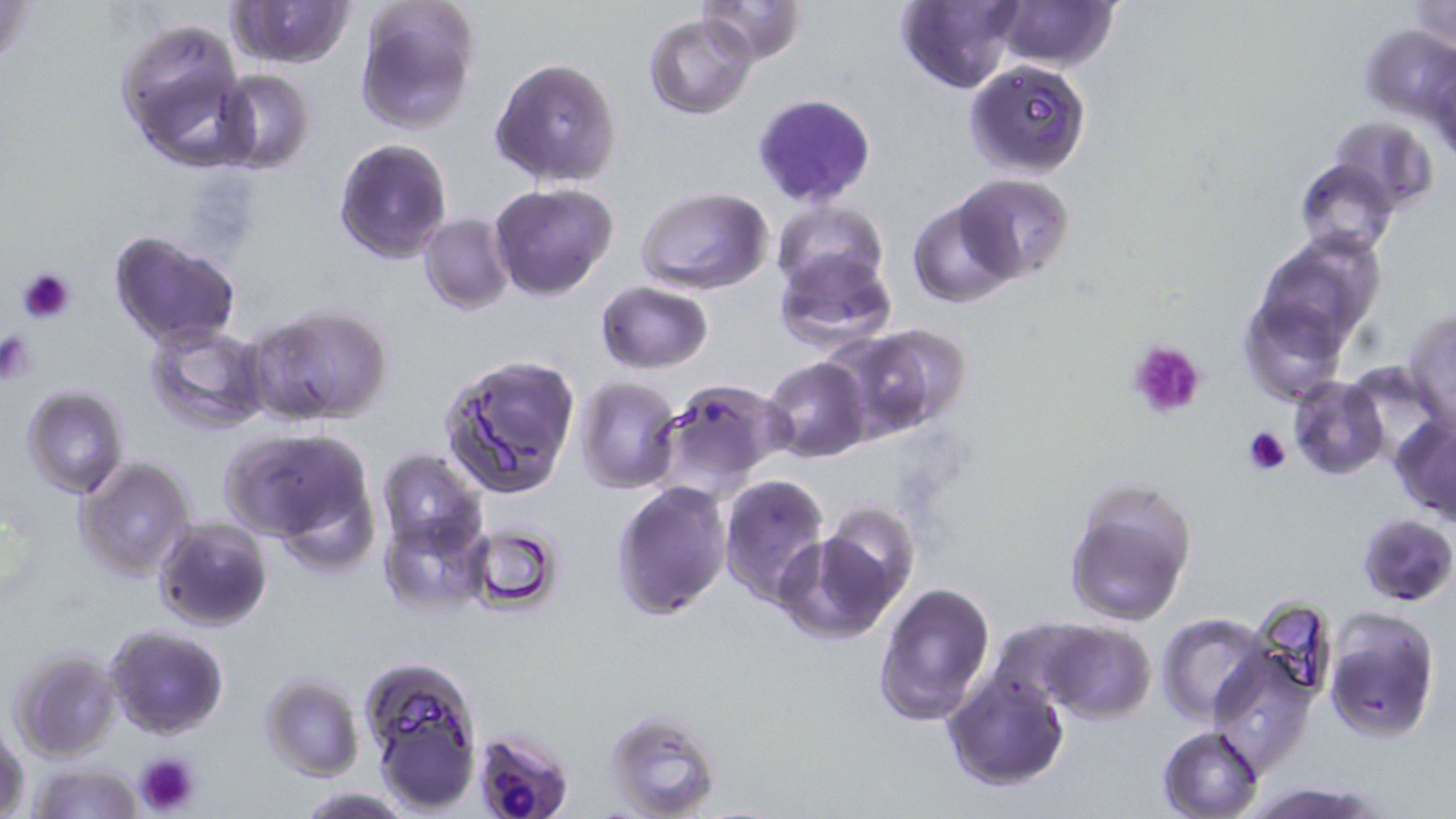
Approximate bounding boxes as named x1/y1/x2/y2 corners in pixels. Uninfected red blood cell locations: (x1=228, y1=0, x2=355, y2=69), (x1=354, y1=0, x2=480, y2=133), (x1=699, y1=0, x2=805, y2=64), (x1=896, y1=0, x2=1023, y2=92), (x1=1406, y1=0, x2=1456, y2=55), (x1=989, y1=1, x2=1123, y2=70), (x1=644, y1=14, x2=757, y2=119), (x1=114, y1=15, x2=249, y2=166), (x1=1357, y1=24, x2=1455, y2=122), (x1=1425, y1=55, x2=1456, y2=166), (x1=490, y1=57, x2=622, y2=188), (x1=965, y1=60, x2=1092, y2=177), (x1=211, y1=70, x2=316, y2=173), (x1=751, y1=93, x2=876, y2=207), (x1=1323, y1=115, x2=1438, y2=211), (x1=334, y1=139, x2=452, y2=262), (x1=1294, y1=159, x2=1399, y2=257), (x1=953, y1=175, x2=1077, y2=282), (x1=489, y1=182, x2=618, y2=299), (x1=634, y1=186, x2=775, y2=294), (x1=908, y1=197, x2=1023, y2=308), (x1=772, y1=201, x2=888, y2=297), (x1=420, y1=213, x2=515, y2=314), (x1=1248, y1=228, x2=1384, y2=364), (x1=108, y1=233, x2=241, y2=349), (x1=772, y1=247, x2=897, y2=353), (x1=595, y1=281, x2=714, y2=373), (x1=1402, y1=304, x2=1456, y2=430), (x1=244, y1=306, x2=394, y2=425), (x1=143, y1=322, x2=272, y2=433), (x1=832, y1=323, x2=971, y2=440), (x1=438, y1=353, x2=580, y2=501), (x1=762, y1=356, x2=871, y2=461), (x1=655, y1=375, x2=791, y2=496), (x1=573, y1=377, x2=683, y2=493), (x1=1286, y1=377, x2=1391, y2=479), (x1=21, y1=385, x2=131, y2=499), (x1=1390, y1=412, x2=1456, y2=524), (x1=222, y1=425, x2=374, y2=548), (x1=376, y1=451, x2=489, y2=555), (x1=75, y1=456, x2=197, y2=582), (x1=718, y1=475, x2=830, y2=607), (x1=1063, y1=479, x2=1196, y2=628), (x1=610, y1=480, x2=731, y2=620), (x1=810, y1=499, x2=926, y2=627), (x1=378, y1=512, x2=491, y2=617), (x1=1357, y1=512, x2=1456, y2=606), (x1=153, y1=516, x2=272, y2=631), (x1=461, y1=524, x2=563, y2=612), (x1=775, y1=527, x2=904, y2=647), (x1=874, y1=583, x2=997, y2=726), (x1=1247, y1=598, x2=1337, y2=702), (x1=1323, y1=608, x2=1441, y2=743), (x1=1157, y1=613, x2=1271, y2=724), (x1=1036, y1=619, x2=1157, y2=723), (x1=105, y1=624, x2=229, y2=740), (x1=10, y1=648, x2=124, y2=762), (x1=1207, y1=650, x2=1318, y2=775), (x1=363, y1=658, x2=481, y2=809), (x1=940, y1=665, x2=1071, y2=790), (x1=260, y1=673, x2=365, y2=781), (x1=603, y1=706, x2=723, y2=819), (x1=1, y1=714, x2=29, y2=818), (x1=1158, y1=725, x2=1265, y2=819), (x1=24, y1=760, x2=144, y2=819), (x1=1241, y1=778, x2=1393, y2=819), (x1=294, y1=787, x2=413, y2=818). Plasmodium falciparum-infected red blood cell locations: (x1=472, y1=728, x2=574, y2=819). Platelet locations: (x1=17, y1=266, x2=76, y2=325), (x1=1, y1=331, x2=37, y2=382), (x1=1124, y1=338, x2=1210, y2=422), (x1=1243, y1=426, x2=1292, y2=476), (x1=133, y1=752, x2=203, y2=819). Slide-level diagnosis: Plasmodium falciparum. Image is 1456×819 pixels. Thin blood smear. Light microscopy. Captured at 1000x magnification. Single field of view. May-Grünwald-Giemsa-stained preparation.